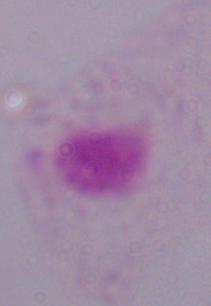

Summary:
  - Identification: trichomonad
  - Magnification: 1000x
  - Modality: micrograph